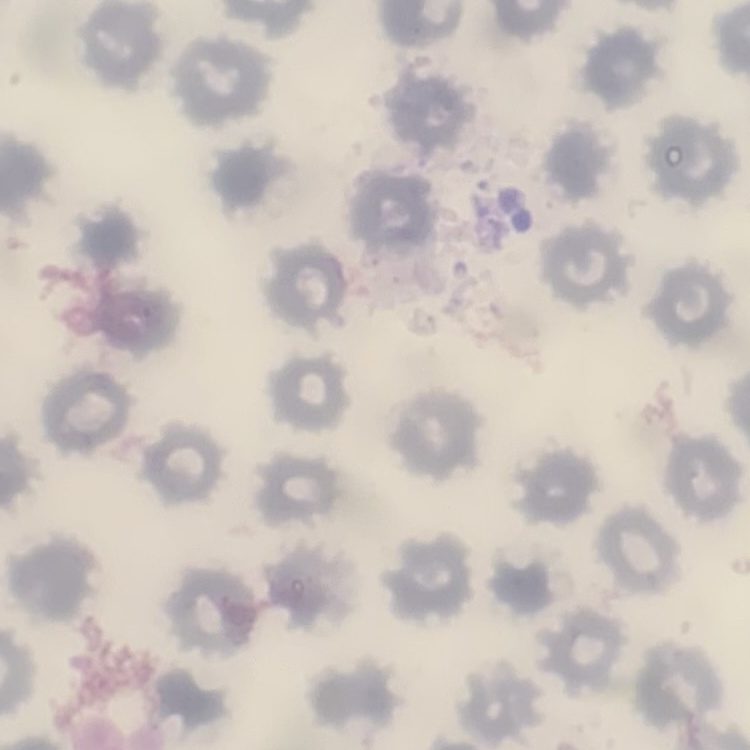

Summary:
  - Erythrocyte morphology: no rouleaux formation
  - Stain: Field's or Giemsa
  - Image type: one tile cut from a larger photomicrograph
  - Preparation: thin blood smear